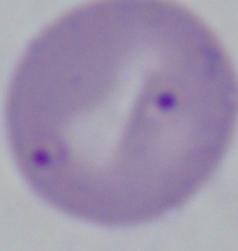
1000x magnification. Micrograph. A Babesia parasite is shown.